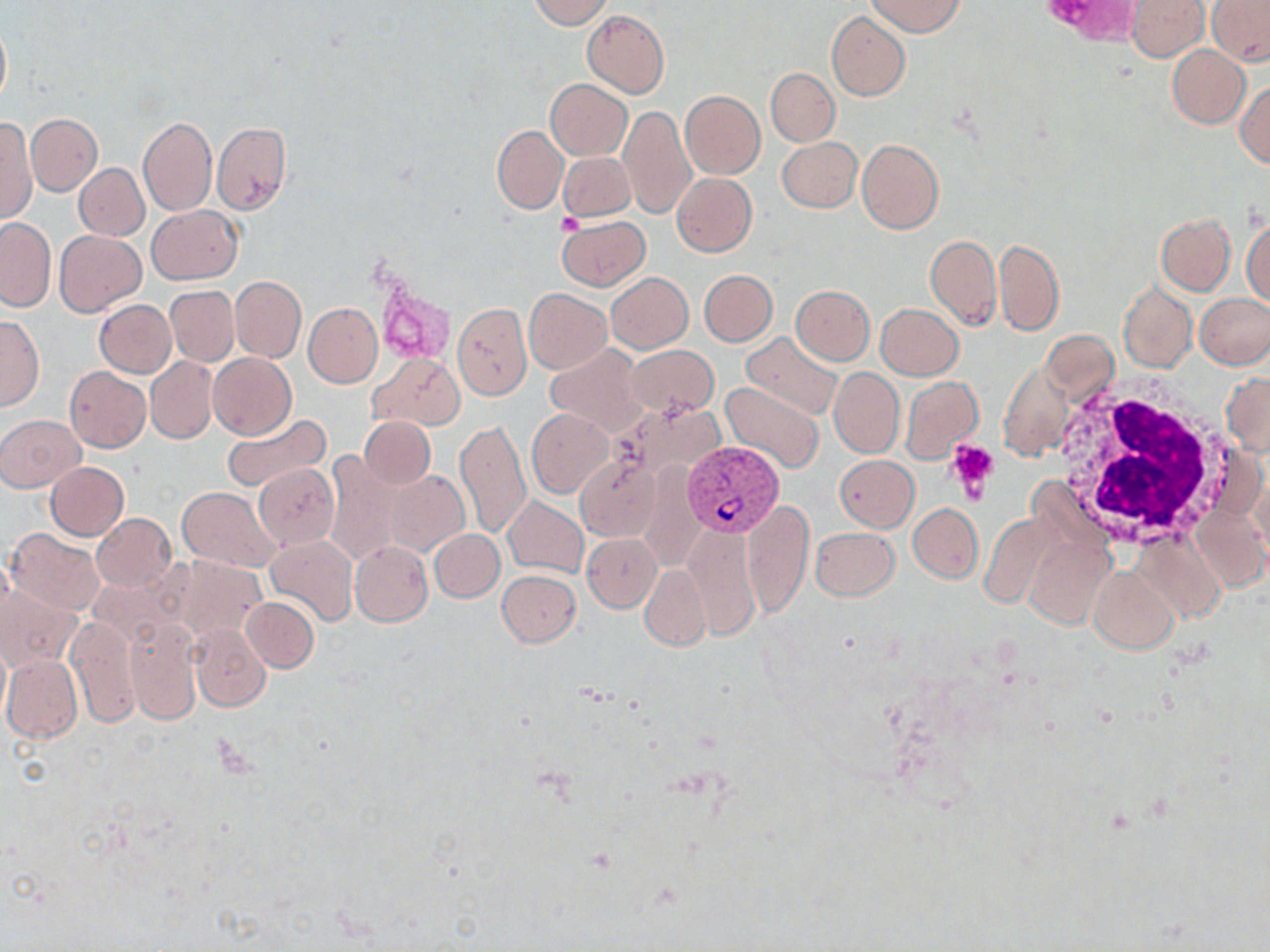

Summary:
  - Coordinate format: approximate bounding boxes as (x1,y1)-(x2,y2) corner pairs in pixels
  - White blood cell locations: (1050,383)-(1230,552)
  - Plasmodium vivax-infected red blood cell locations: (683,440)-(784,537)
  - Uninfected red blood cell locations: (529,0)-(614,28), (867,0)-(964,36), (1126,0)-(1209,62), (1206,0)-(1270,65), (582,9)-(669,97), (827,11)-(910,101), (0,14)-(11,110), (1168,45)-(1251,129), (766,68)-(839,147), (546,79)-(633,160), (1235,80)-(1270,168), (680,90)-(765,180), (619,106)-(695,219), (26,113)-(102,196), (1,115)-(36,225), (138,116)-(217,216), (212,121)-(292,213), (492,125)-(568,214), (777,136)-(862,213), (856,139)-(943,234), (558,152)-(635,222), (75,163)-(148,241), (672,173)-(757,257), (146,205)-(243,285), (1242,213)-(1270,307), (1155,214)-(1234,294), (558,215)-(650,290), (0,216)-(55,313), (54,231)-(145,316), (926,234)-(1001,329), (994,239)-(1064,335), (700,269)-(777,346), (605,272)-(692,353), (230,276)-(305,362), (1118,280)-(1196,374), (790,284)-(875,365), (165,286)-(239,367), (524,288)-(612,373), (1195,292)-(1270,368), (94,299)-(176,377), (452,302)-(532,400), (303,303)-(383,387), (875,303)-(965,380), (81,304)-(166,450), (0,315)-(43,410), (1041,330)-(1119,406), (740,331)-(842,420), (545,344)-(646,436), (626,345)-(718,417), (208,353)-(296,439), (368,353)-(464,431), (146,357)-(219,444), (999,361)-(1075,461), (64,367)-(151,452), (829,368)-(904,458), (1221,372)-(1270,457), (899,375)-(983,464), (720,381)-(823,473), (526,408)-(615,499), (220,412)-(333,494), (0,413)-(85,492), (359,416)-(435,490), (455,420)-(531,538), (576,453)-(662,541), (324,454)-(404,571), (835,455)-(918,532), (44,461)-(129,540), (254,464)-(339,549), (384,469)-(469,556), (176,486)-(281,571), (503,496)-(588,578), (741,499)-(813,619), (1191,501)-(1268,592), (908,503)-(983,582), (978,511)-(1062,611), (91,513)-(176,592), (683,524)-(760,641), (810,527)-(900,601), (8,529)-(104,616), (429,529)-(505,602), (1130,530)-(1227,626), (582,533)-(661,611), (1025,533)-(1115,630), (265,534)-(358,626), (351,541)-(433,627), (167,556)-(269,642), (640,564)-(710,650), (1088,566)-(1179,653), (497,569)-(582,647), (1,582)-(82,671), (241,596)-(319,672), (125,615)-(200,724), (66,616)-(140,728), (189,625)-(271,712), (2,655)-(83,742)
  - Platelet locations: (557,214)-(581,236), (946,439)-(999,498)
  - Slide-level diagnosis: Plasmodium vivax
  - Stain: May-Grünwald-Giemsa
  - Magnification: 1000x
  - Field of view: single
  - Modality: light microscopy
  - Image size: 1270×952 pixels
  - Preparation: thin blood film